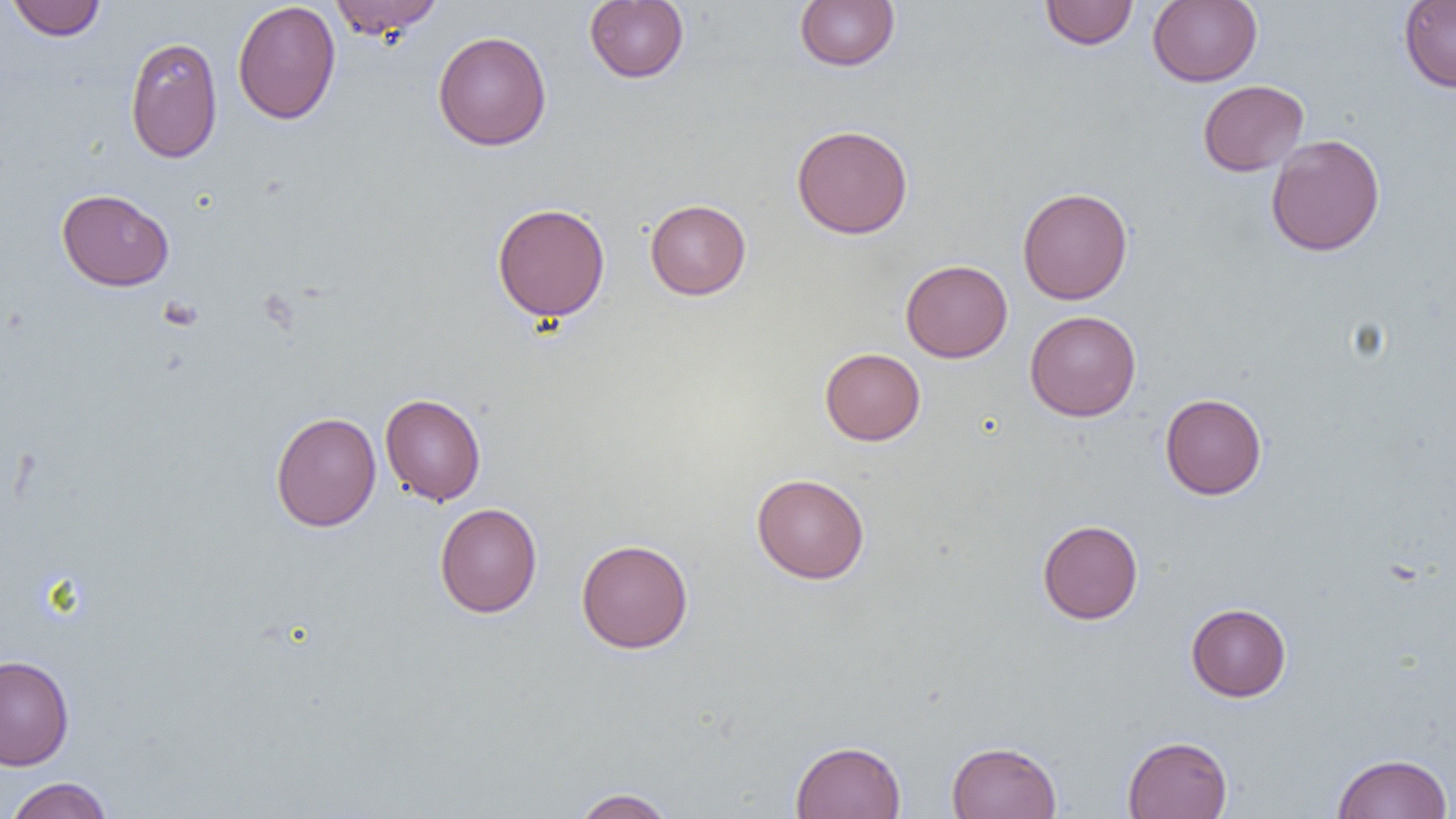

slide_level_diagnosis: no evidence of blood parasites
magnification: 1000x
preparation: thin blood smear
modality: light microscopy
image_size: 1456×819 pixels
uninfected_red_blood_cell_locations: 'approximate bounding boxes as (x1,y1)-(x2,y2) corner pairs in pixels: (6,0)-(107,41), (329,0)-(444,40), (584,0)-(689,83), (795,0)-(900,71), (1147,0)-(1262,87), (1399,0)-(1456,92), (232,1)-(341,125), (1039,1)-(1138,49), (433,30)-(552,151), (125,37)-(223,163), (1197,80)-(1308,176), (791,124)-(913,239), (1265,133)-(1385,256), (1017,187)-(1133,304), (56,188)-(174,291), (645,199)-(751,300), (492,203)-(611,322), (900,259)-(1013,362), (1025,310)-(1141,421), (820,348)-(925,446), (380,393)-(486,505), (1160,393)-(1267,500), (270,411)-(381,532), (751,473)-(869,584), (434,502)-(542,618), (1037,519)-(1143,624), (576,538)-(693,653), (1186,602)-(1291,701), (0,654)-(74,770), (1122,735)-(1232,819), (790,740)-(906,818), (947,740)-(1062,819), (1332,753)-(1453,819), (4,776)-(115,819), (571,787)-(676,818)'
field_of_view: single